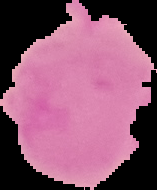
Summary:
  - Preparation: thin blood smear
  - Image type: segmented cell region on a black background
  - Image size: 157×190 pixels
  - Malaria status: uninfected